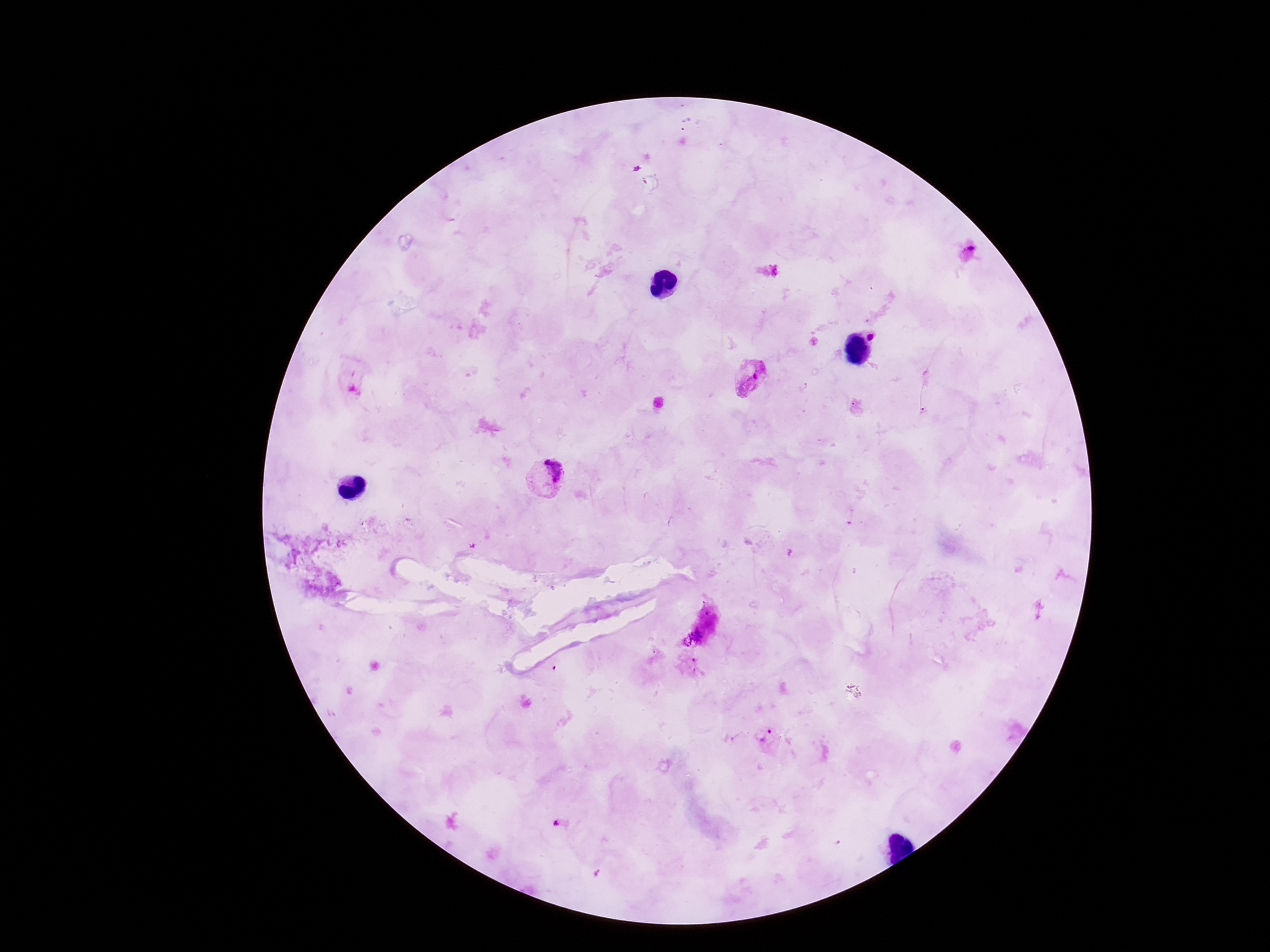
Approximate centers as [x, y] in pixels.
Summary:
  - Plasmodium parasite locations: [871, 337], [752, 382], [353, 383], [545, 476], [769, 738], [558, 824]
  - Patient malaria status: infected
  - Magnification: 100x
  - Capture: smartphone camera through the microscope eyepiece
  - Field of view: single
  - Stain: Giemsa
  - Image size: 1270×952 pixels
  - Preparation: thick blood smear